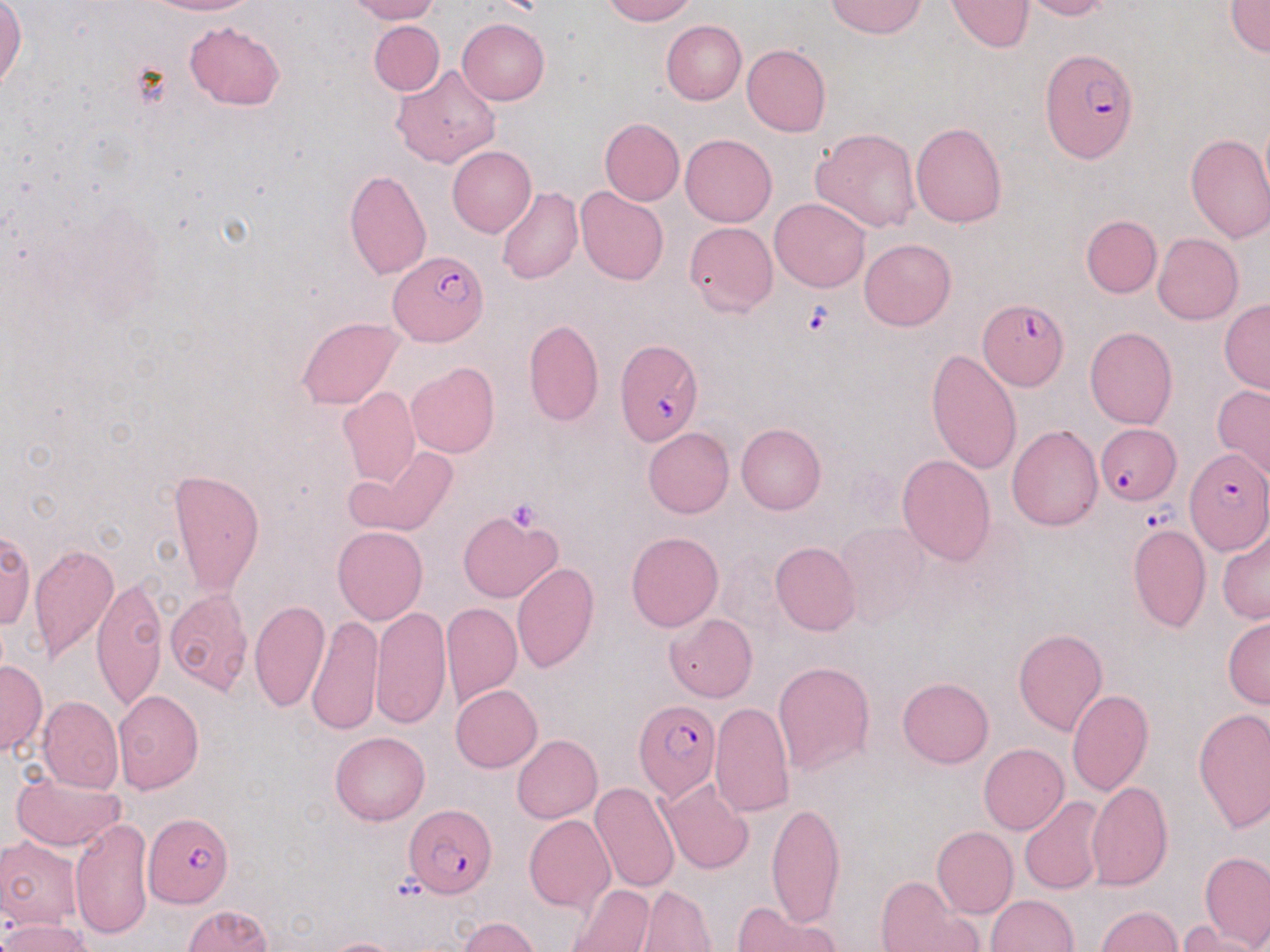
Approximate bounding boxes as named x1/y1/x2/y2 corners in pixels. Platelet locations: (x1=504, y1=498, x2=544, y2=531). Plasmodium falciparum-infected red blood cell locations: (x1=1040, y1=49, x2=1139, y2=162), (x1=390, y1=250, x2=487, y2=346), (x1=978, y1=298, x2=1069, y2=391), (x1=614, y1=339, x2=703, y2=447), (x1=1095, y1=424, x2=1181, y2=505), (x1=1184, y1=447, x2=1268, y2=554), (x1=635, y1=700, x2=721, y2=802), (x1=406, y1=804, x2=496, y2=898), (x1=144, y1=812, x2=232, y2=909). Uninfected red blood cell locations: (x1=142, y1=0, x2=258, y2=17), (x1=342, y1=0, x2=439, y2=24), (x1=602, y1=0, x2=696, y2=24), (x1=826, y1=0, x2=927, y2=39), (x1=947, y1=0, x2=1033, y2=52), (x1=1021, y1=0, x2=1114, y2=21), (x1=1226, y1=0, x2=1270, y2=56), (x1=0, y1=1, x2=25, y2=94), (x1=458, y1=18, x2=550, y2=104), (x1=661, y1=19, x2=746, y2=104), (x1=184, y1=20, x2=285, y2=110), (x1=369, y1=21, x2=445, y2=96), (x1=741, y1=45, x2=831, y2=137), (x1=392, y1=66, x2=501, y2=169), (x1=599, y1=118, x2=684, y2=206), (x1=910, y1=121, x2=1006, y2=228), (x1=811, y1=128, x2=922, y2=232), (x1=1185, y1=133, x2=1270, y2=242), (x1=679, y1=134, x2=776, y2=226), (x1=448, y1=145, x2=537, y2=237), (x1=344, y1=170, x2=432, y2=281), (x1=497, y1=187, x2=582, y2=284), (x1=575, y1=187, x2=669, y2=286), (x1=769, y1=198, x2=870, y2=292), (x1=1081, y1=215, x2=1161, y2=297), (x1=684, y1=220, x2=777, y2=317), (x1=1153, y1=233, x2=1244, y2=324), (x1=859, y1=237, x2=956, y2=330), (x1=1219, y1=300, x2=1270, y2=394), (x1=296, y1=316, x2=403, y2=410), (x1=523, y1=319, x2=604, y2=426), (x1=1085, y1=327, x2=1178, y2=429), (x1=926, y1=348, x2=1021, y2=477), (x1=407, y1=363, x2=499, y2=457), (x1=1212, y1=384, x2=1270, y2=482), (x1=336, y1=385, x2=420, y2=487), (x1=736, y1=424, x2=826, y2=514), (x1=1007, y1=425, x2=1103, y2=532), (x1=643, y1=427, x2=733, y2=519), (x1=347, y1=445, x2=457, y2=537), (x1=896, y1=454, x2=997, y2=566), (x1=167, y1=468, x2=265, y2=596), (x1=458, y1=511, x2=562, y2=604), (x1=834, y1=521, x2=928, y2=628), (x1=1126, y1=524, x2=1211, y2=632), (x1=332, y1=525, x2=427, y2=625), (x1=1217, y1=528, x2=1270, y2=625), (x1=0, y1=529, x2=34, y2=631), (x1=626, y1=531, x2=723, y2=630), (x1=28, y1=541, x2=118, y2=662), (x1=770, y1=541, x2=859, y2=636), (x1=511, y1=562, x2=599, y2=674), (x1=92, y1=574, x2=168, y2=708), (x1=164, y1=589, x2=253, y2=694), (x1=249, y1=599, x2=328, y2=712), (x1=441, y1=603, x2=521, y2=706), (x1=370, y1=605, x2=451, y2=731), (x1=665, y1=613, x2=757, y2=702), (x1=308, y1=616, x2=384, y2=735), (x1=1223, y1=616, x2=1270, y2=707), (x1=1013, y1=628, x2=1107, y2=736), (x1=0, y1=659, x2=46, y2=756), (x1=773, y1=660, x2=875, y2=777), (x1=896, y1=677, x2=994, y2=768), (x1=451, y1=683, x2=542, y2=771), (x1=1066, y1=688, x2=1154, y2=796), (x1=112, y1=689, x2=204, y2=794), (x1=37, y1=696, x2=123, y2=793), (x1=710, y1=702, x2=793, y2=819), (x1=1193, y1=709, x2=1270, y2=832), (x1=330, y1=731, x2=429, y2=825), (x1=512, y1=735, x2=602, y2=822), (x1=978, y1=744, x2=1068, y2=834), (x1=10, y1=769, x2=126, y2=853), (x1=659, y1=779, x2=755, y2=876), (x1=1087, y1=781, x2=1173, y2=892), (x1=590, y1=782, x2=681, y2=892), (x1=1020, y1=797, x2=1108, y2=895), (x1=766, y1=798, x2=845, y2=929), (x1=524, y1=814, x2=616, y2=914), (x1=69, y1=817, x2=154, y2=940), (x1=931, y1=825, x2=1018, y2=918), (x1=0, y1=836, x2=84, y2=932), (x1=1201, y1=851, x2=1269, y2=951), (x1=876, y1=876, x2=974, y2=951), (x1=568, y1=883, x2=655, y2=952), (x1=636, y1=885, x2=717, y2=952), (x1=986, y1=894, x2=1078, y2=952), (x1=732, y1=902, x2=842, y2=952), (x1=182, y1=904, x2=272, y2=952), (x1=1095, y1=905, x2=1183, y2=952), (x1=2, y1=916, x2=91, y2=952), (x1=457, y1=917, x2=541, y2=952), (x1=1177, y1=924, x2=1265, y2=952), (x1=323, y1=938, x2=406, y2=952). Slide-level diagnosis: Plasmodium falciparum. Captured at 1000x magnification. Single field of view. Image is 1270×952 pixels. Thin blood film. Light microscopy. May-Grünwald-Giemsa stain.